Classify this cell by malaria status.
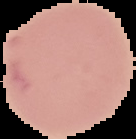
It is uninfected.

Segmented cell region on a black background. From a thin blood smear. Image is 136×139 pixels.